Report the malaria status of this cell.
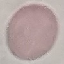

Uninfected.

Thin blood film. Giemsa stain. Acquired by smartphone through the microscope eyepiece. Automatically extracted cell patch, resized to 64 × 64 pixels.